State the blood parasite species.
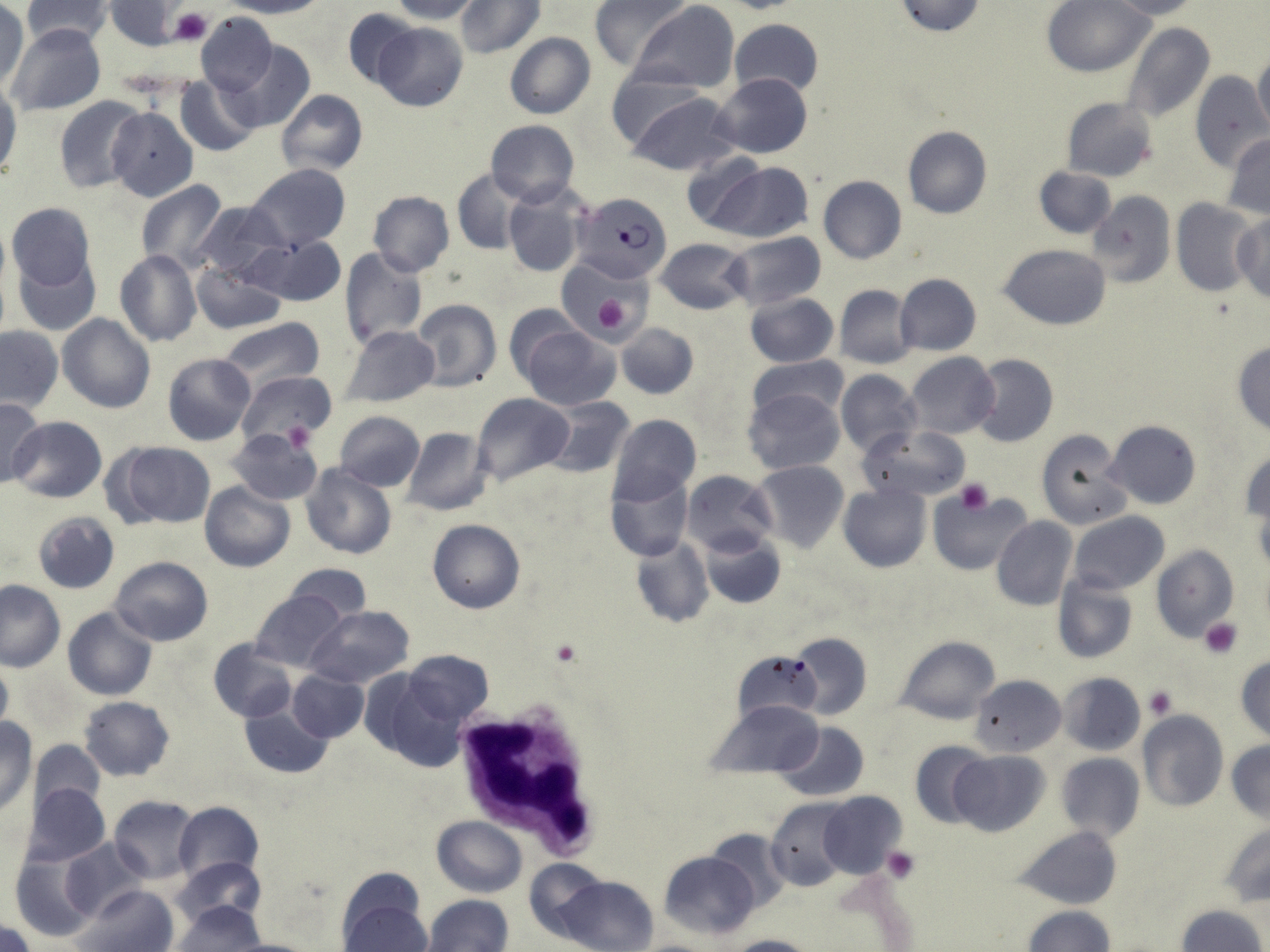

Plasmodium falciparum.

preparation: thin blood film
plasmodium_falciparum_infected_red_blood_cell_locations: 'approximate bounding boxes as (x1, y1, x2, y2) in pixels: (576, 191, 672, 283)'
modality: optical microscopy
white_blood_cell_locations: 'approximate bounding boxes as (x1, y1, x2, y2) in pixels: (446, 699, 607, 860)'
field_of_view: single
stain: May-Grünwald-Giemsa
magnification: 1000x
uninfected_red_blood_cell_locations: 'approximate bounding boxes as (x1, y1, x2, y2) in pixels: (19, 0, 114, 48), (226, 0, 327, 18), (389, 0, 484, 23), (456, 0, 545, 58), (588, 0, 689, 72), (715, 0, 807, 13), (893, 0, 987, 37), (1044, 0, 1154, 77), (632, 1, 740, 93), (1104, 1, 1202, 20), (0, 2, 29, 92), (107, 2, 187, 51), (344, 9, 418, 89), (195, 12, 277, 97), (728, 19, 824, 100), (1121, 21, 1216, 126), (372, 23, 467, 112), (6, 24, 106, 116), (504, 33, 596, 119), (225, 41, 317, 134), (1252, 52, 1270, 138), (605, 68, 710, 148), (1189, 70, 1268, 171), (713, 73, 812, 158), (175, 75, 259, 155), (0, 79, 19, 184), (277, 89, 368, 178), (628, 93, 739, 177), (55, 97, 146, 193), (1060, 97, 1159, 182), (106, 107, 198, 202), (485, 120, 579, 207), (902, 126, 992, 219), (1224, 134, 1270, 220), (679, 150, 767, 233), (706, 161, 814, 243), (244, 164, 351, 252), (1033, 167, 1116, 239), (452, 169, 530, 254), (817, 175, 906, 264), (135, 180, 229, 272), (502, 184, 589, 278), (1086, 189, 1175, 289), (368, 191, 454, 277), (1170, 198, 1257, 297), (193, 199, 290, 284), (7, 203, 96, 291), (1232, 214, 1270, 305), (724, 231, 826, 309), (248, 234, 346, 307), (656, 237, 753, 314), (1000, 244, 1112, 330), (338, 248, 428, 350), (13, 250, 101, 336), (114, 250, 202, 347), (191, 261, 285, 334), (76, 273, 175, 390), (894, 273, 982, 356), (834, 285, 916, 368), (744, 291, 838, 368), (410, 299, 501, 391), (504, 305, 582, 385), (57, 313, 154, 413), (216, 319, 326, 393), (615, 323, 698, 399), (0, 325, 63, 413), (340, 325, 440, 408), (520, 327, 621, 411), (1231, 341, 1270, 437), (905, 351, 1000, 439), (162, 353, 256, 446), (972, 353, 1058, 447), (746, 356, 850, 422), (735, 362, 901, 448), (835, 370, 923, 459), (236, 371, 336, 449), (743, 388, 845, 476), (471, 393, 574, 486), (542, 396, 636, 479), (0, 398, 45, 487), (334, 411, 425, 490), (609, 414, 701, 506), (8, 415, 108, 503), (1104, 419, 1202, 510), (857, 424, 970, 503), (404, 427, 492, 516), (1034, 428, 1133, 528), (226, 429, 323, 506), (108, 440, 218, 529), (1241, 446, 1269, 532), (753, 461, 850, 553), (301, 464, 396, 560), (682, 469, 778, 559), (604, 472, 692, 563), (201, 482, 295, 572), (839, 484, 931, 572), (928, 487, 1028, 575), (1254, 496, 1270, 579), (32, 510, 121, 594), (1069, 512, 1170, 594), (992, 517, 1078, 612), (428, 519, 525, 614), (699, 529, 786, 608), (630, 537, 713, 629), (1151, 546, 1239, 643), (110, 556, 214, 646), (284, 564, 372, 625), (1052, 575, 1138, 664), (0, 580, 65, 671), (248, 588, 349, 672), (62, 606, 157, 701), (304, 606, 414, 688), (789, 633, 872, 719), (895, 636, 1000, 724), (208, 638, 297, 724), (733, 648, 823, 729), (402, 651, 495, 727), (0, 655, 13, 736), (1234, 656, 1270, 741), (286, 670, 369, 742), (1057, 672, 1145, 755), (969, 674, 1065, 757), (366, 675, 467, 772), (78, 696, 175, 781), (705, 699, 824, 776), (237, 700, 334, 781), (1137, 711, 1229, 814), (1, 719, 36, 814), (775, 722, 868, 800), (29, 740, 104, 813), (909, 740, 991, 828), (1227, 741, 1270, 824), (949, 750, 1050, 837), (1055, 753, 1145, 842), (23, 783, 111, 866), (818, 792, 908, 879), (109, 796, 199, 882), (767, 798, 850, 889), (173, 801, 263, 882), (432, 816, 526, 896), (1219, 824, 1270, 907), (1015, 827, 1123, 908), (707, 829, 791, 912), (60, 838, 150, 920), (659, 850, 759, 941), (10, 852, 100, 942), (172, 857, 267, 932), (524, 858, 607, 942), (558, 876, 658, 952), (72, 884, 178, 952), (423, 894, 516, 952), (171, 901, 266, 950), (342, 901, 431, 952), (1178, 904, 1266, 952), (1024, 907, 1113, 952), (0, 920, 37, 952), (723, 934, 819, 952), (216, 937, 320, 952)'
image_size: 1270×952 pixels
platelet_locations: 'approximate bounding boxes as (x1, y1, x2, y2) in pixels: (168, 7, 211, 45), (590, 291, 635, 338), (280, 419, 314, 455), (956, 480, 994, 513), (1200, 617, 1243, 657), (550, 641, 583, 667), (1144, 685, 1178, 720), (882, 848, 920, 883)'